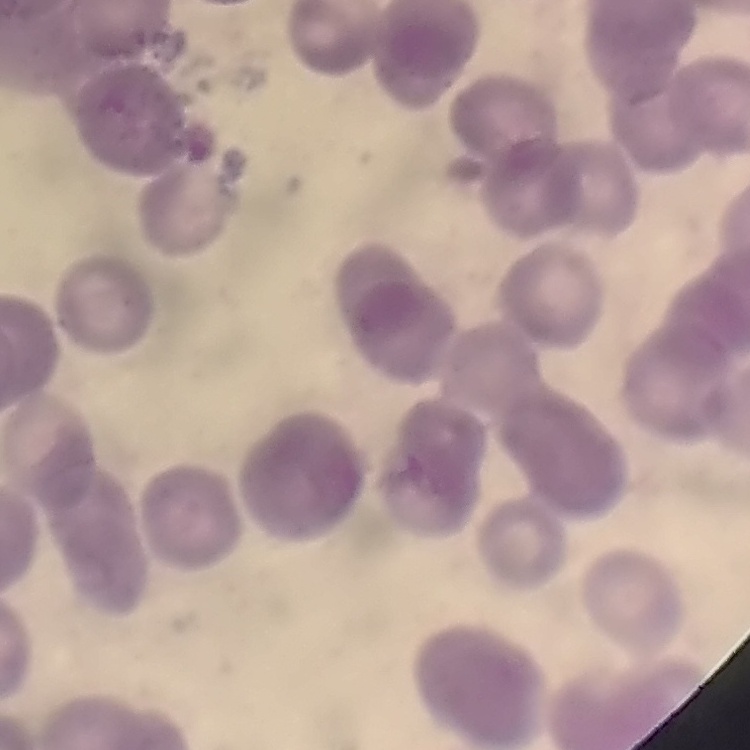

red_blood_cell_morphology: rouleaux formation
preparation: thin peripheral smear
stain: Field's or Giemsa
image_type: square crop of a larger photomicrograph